Classify this cell by malaria status.
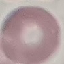
Uninfected.

stain = Giemsa
preparation = thin blood film
capture = smartphone through the microscope eyepiece
image type = cell patch, automatically extracted from a larger field of view and resized to 64 × 64 pixels